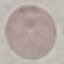
Malaria status: uninfected. Giemsa stain. Photographed with a smartphone camera at the microscope eyepiece. Automatically extracted cell patch, resized to 64 × 64 pixels. Thin blood smear.